Find the cells and give the type of each one.
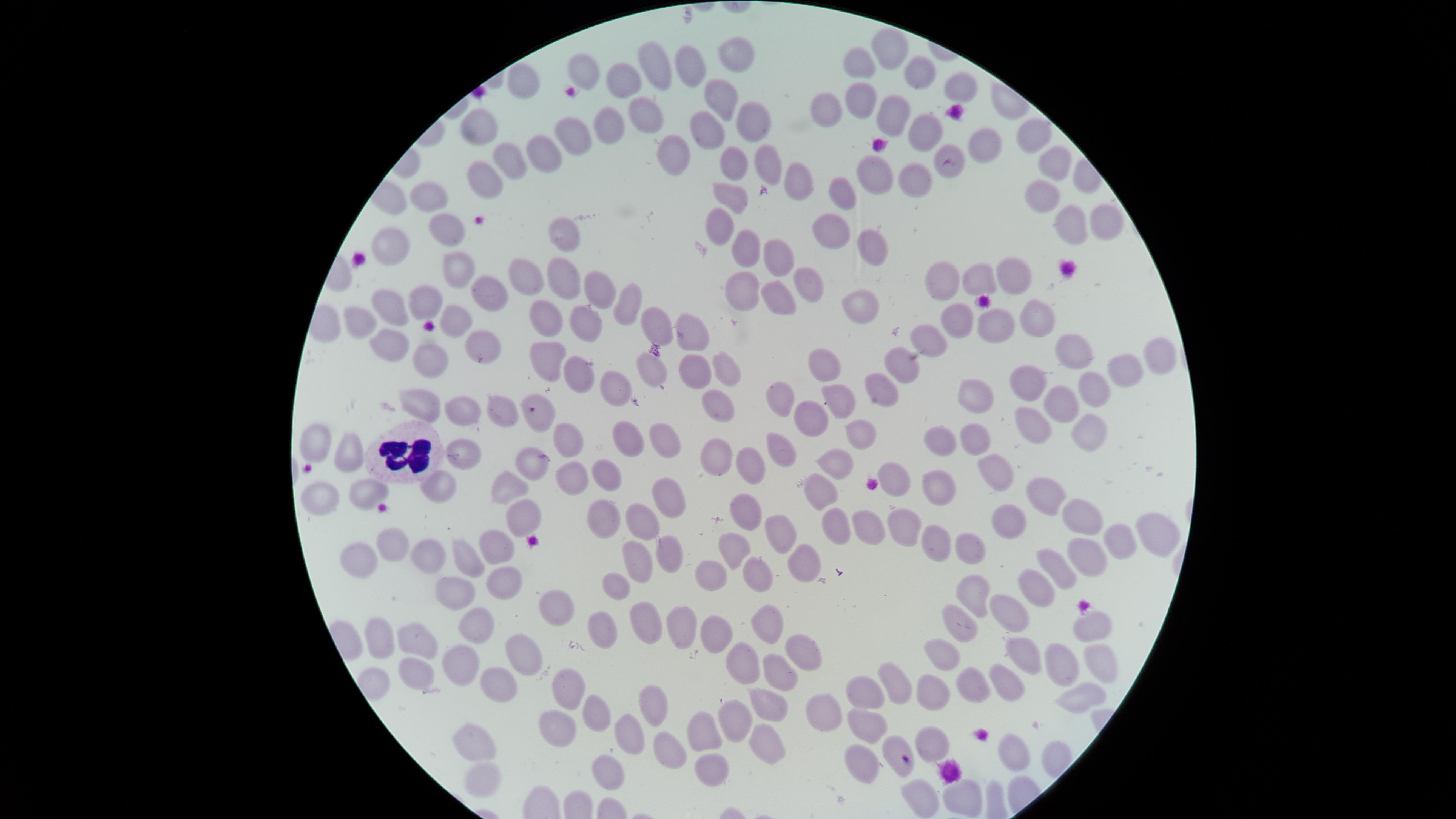
No parasitized red blood cells identified.
Approximate marker points as {x, y} in pixels.
Uninfected red blood cells: {895, 47}, {730, 53}, {659, 61}, {691, 64}, {865, 65}, {588, 69}, {917, 71}, {627, 79}, {526, 81}, {961, 87}, {857, 93}, {717, 94}, {826, 105}, {888, 109}, {645, 113}, {742, 115}, {916, 124}, {485, 126}, {601, 128}, {702, 132}, {1033, 133}, {574, 134}, {983, 144}, {674, 146}, {545, 150}, {761, 161}, {511, 162}, {731, 163}, {1051, 163}, {948, 164}, {912, 169}, {485, 173}, {874, 173}, {797, 178}, {843, 191}, {732, 197}, {429, 198}, {1036, 200}, {1104, 219}, {1072, 221}, {834, 222}, {722, 225}, {448, 226}, {559, 233}, {867, 244}, {391, 246}, {745, 246}, {776, 250}, {460, 261}, {1004, 269}, {528, 273}, {943, 274}, {559, 275}, {972, 276}, {803, 283}, {599, 289}, {741, 289}, {486, 290}, {417, 295}, {774, 295}, {625, 300}, {858, 305}, {387, 309}, {1039, 313}, {547, 316}, {957, 317}, {459, 318}, {650, 319}, {362, 320}, {998, 323}, {586, 324}, {687, 326}, {935, 333}, {392, 345}, {476, 345}, {1073, 347}, {1150, 355}, {550, 356}, {431, 357}, {906, 362}, {652, 364}, {826, 364}, {691, 366}, {582, 368}, {1121, 368}, {721, 369}, {1029, 383}, {609, 385}, {1092, 386}, {873, 388}, {971, 393}, {780, 395}, {837, 398}, {714, 402}, {421, 403}, {1058, 405}, {509, 406}, {540, 407}, {461, 411}, {806, 414}, {1029, 421}, {1088, 423}, {973, 432}, {860, 433}, {573, 434}, {662, 434}, {934, 434}, {317, 439}, {620, 442}, {778, 442}, {344, 450}, {461, 451}, {719, 453}, {836, 460}, {532, 461}, {756, 462}, {992, 469}, {579, 473}, {603, 474}, {896, 481}, {937, 486}, {434, 488}, {505, 488}, {819, 489}, {362, 492}, {670, 492}, {1041, 493}, {323, 497}, {1084, 512}, {749, 513}, {520, 515}, {609, 516}, {1000, 518}, {642, 521}, {867, 521}, {896, 523}, {831, 525}, {1157, 533}, {782, 536}, {1118, 538}, {397, 541}, {934, 545}, {495, 547}, {972, 547}, {735, 549}, {667, 550}, {1087, 551}, {640, 553}, {429, 554}, {352, 558}, {465, 559}, {1058, 560}, {714, 568}, {802, 569}, {502, 575}, {756, 576}, {614, 582}, {1036, 582}, {977, 591}, {450, 592}, {547, 607}, {1011, 613}, {640, 617}, {767, 618}, {678, 628}, {1090, 628}, {712, 629}, {474, 632}, {598, 634}, {960, 635}, {419, 637}, {381, 641}, {802, 643}, {1020, 650}, {942, 651}, {522, 653}, {738, 658}, {1097, 659}, {1059, 660}, {777, 663}, {464, 664}, {417, 676}, {1005, 677}, {974, 682}, {497, 686}, {562, 689}, {894, 689}, {1080, 691}, {934, 693}, {869, 694}, {767, 698}, {650, 703}, {827, 708}, {595, 710}, {735, 717}, {865, 718}, {555, 725}, {706, 735}, {763, 736}, {478, 738}, {627, 738}, {928, 738}, {901, 741}, {668, 747}, {1010, 751}, {862, 757}, {606, 770}, {709, 773}, {478, 775}, {925, 792}, {961, 796}.
White blood cells: {400, 452}.

visible region = circular
preparation = thin blood film
image size = 1456×819 pixels
field of view = single
capture = smartphone photograph through the microscope eyepiece
stain = Giemsa